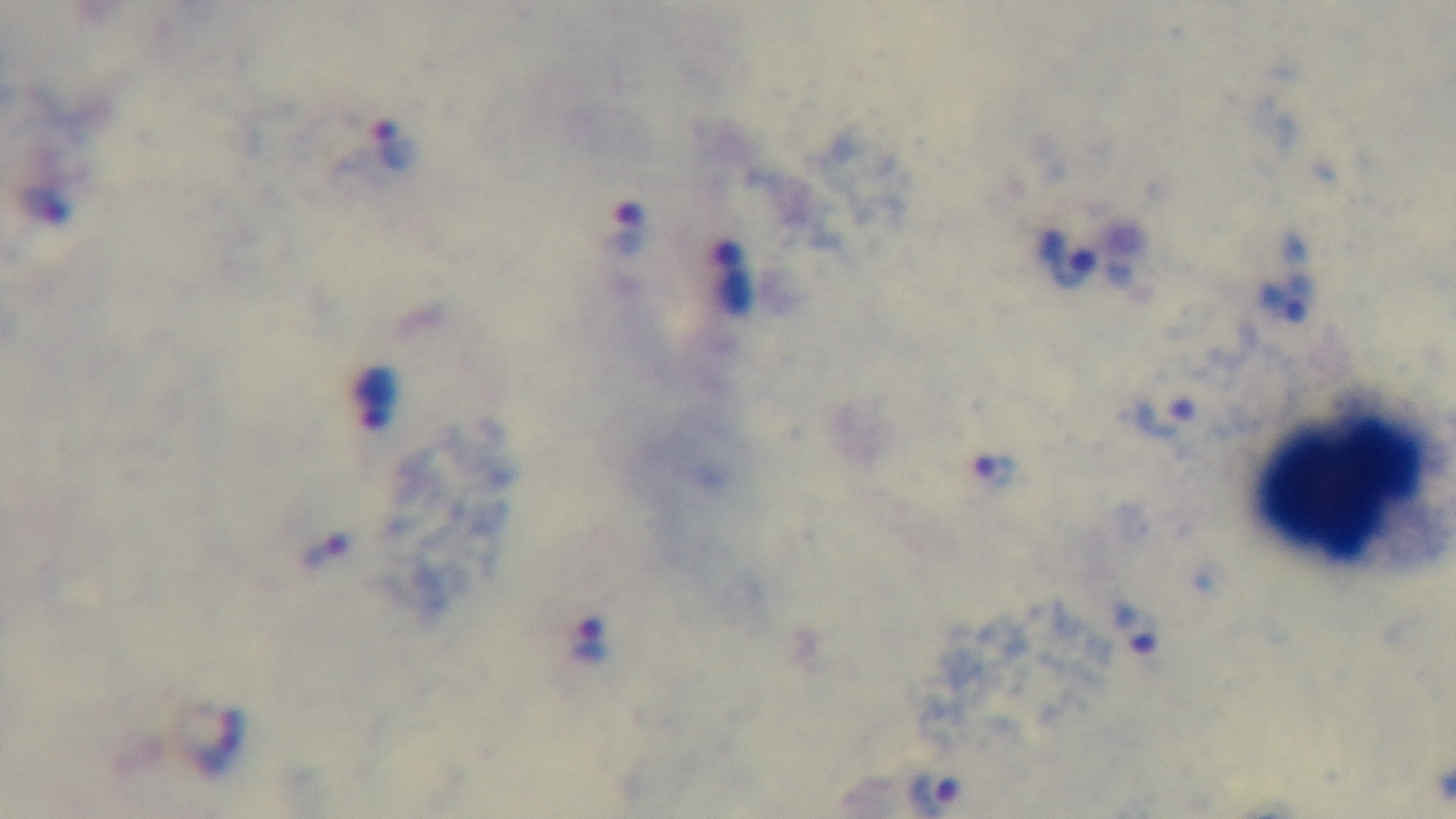

capture = mounted 4K digital camera
malaria status = positive
modality = light microscopy
stain = Giemsa
field of view = single
objective = 100x oil immersion
preparation = thick smear